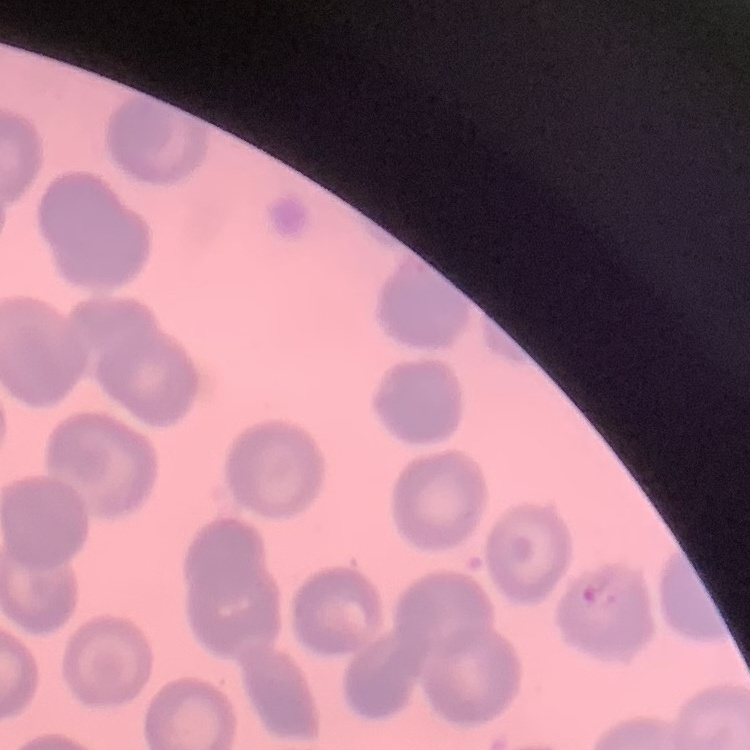

Summary:
  - Erythrocyte morphology: no rouleaux formation
  - Image type: square crop of a larger photomicrograph
  - Stain: Field's or Giemsa
  - Preparation: thin peripheral smear